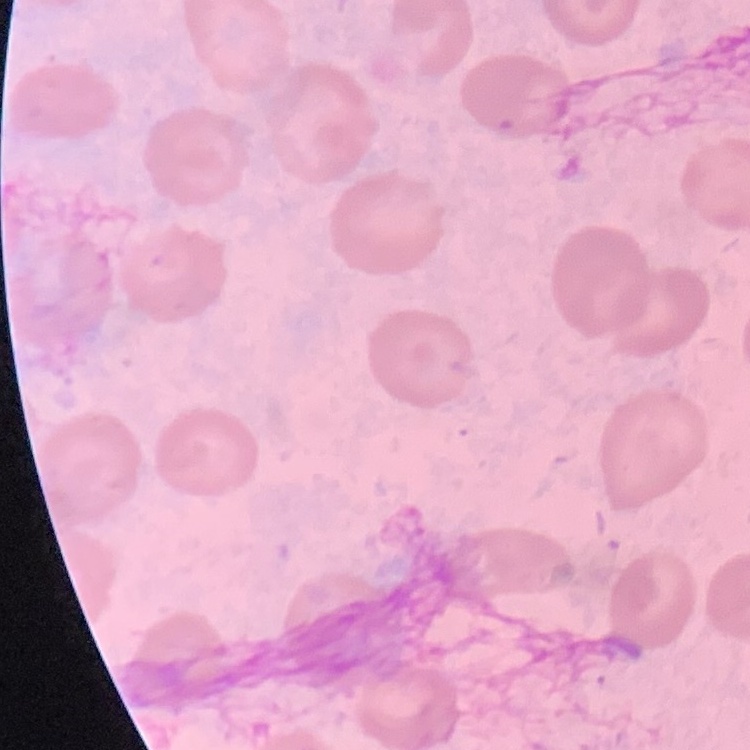

The red blood cells show no rouleaux formation. Thin blood film. Square crop of a larger photomicrograph. Stained with either Field's or Giemsa.